Identify the parasite.
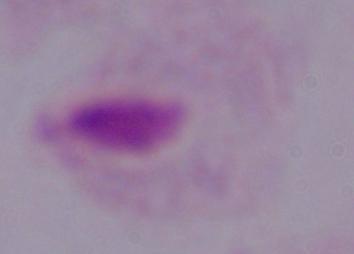

This is a trichomonad.

1000x magnification. Photomicrograph.